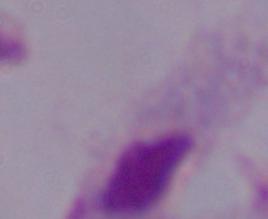
Summary:
  - Identification: trichomonad
  - Magnification: 1000x
  - Modality: photomicrograph